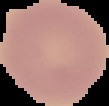
From a thin blood smear. Result: no Plasmodium parasites seen. Image is 109×106 pixels. The area outside the segmented cell region is set to black.